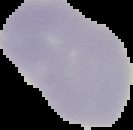
Result: no Plasmodium parasites detected. From a thin blood film. Image is 133×130 pixels. Segmented cell region on a black background.